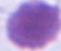

magnification = 1000x
identification = erythrocyte
modality = photomicrograph